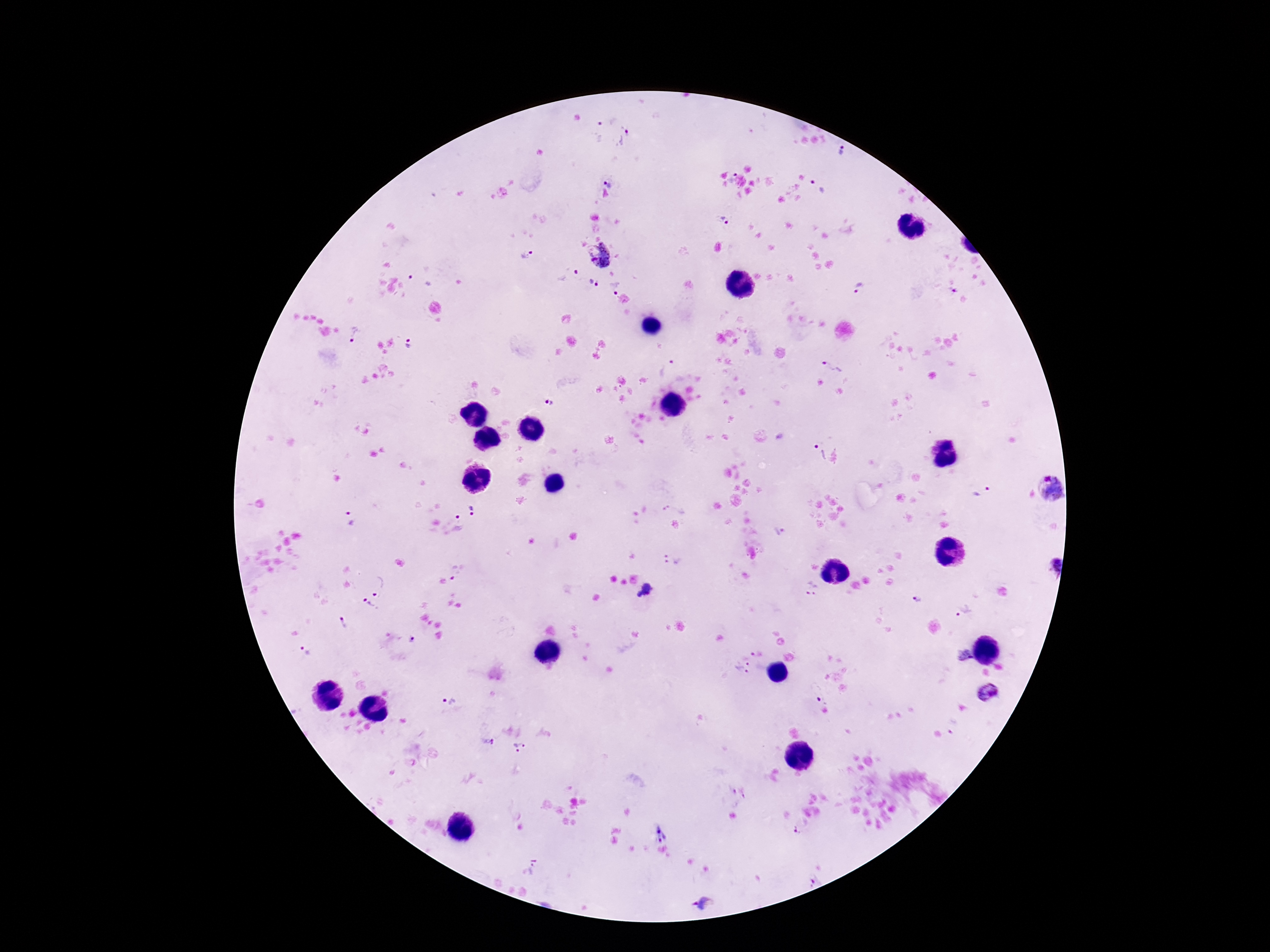
{
  "patient_malaria_status": "positive",
  "image_size": "1270×952 pixels",
  "stain": "Giemsa",
  "field_of_view": "single",
  "plasmodium_parasite_locations": "approximate object centers, in pixels from the top-left corner: (x=598, y=130), (x=627, y=138), (x=843, y=151), (x=731, y=176), (x=610, y=180), (x=819, y=185), (x=724, y=220), (x=597, y=253), (x=528, y=254), (x=567, y=275), (x=420, y=279), (x=592, y=283), (x=616, y=287), (x=858, y=288), (x=951, y=291), (x=354, y=336), (x=409, y=343), (x=666, y=366), (x=832, y=366), (x=551, y=403), (x=816, y=451), (x=1051, y=488), (x=982, y=490), (x=678, y=507), (x=474, y=510), (x=351, y=518), (x=459, y=520), (x=780, y=532), (x=672, y=560), (x=1054, y=565), (x=458, y=571), (x=382, y=584), (x=646, y=588), (x=812, y=588), (x=918, y=598), (x=367, y=606), (x=964, y=611), (x=345, y=621), (x=414, y=640), (x=305, y=652), (x=751, y=654), (x=965, y=656), (x=742, y=667), (x=988, y=692), (x=449, y=700), (x=488, y=743), (x=519, y=747), (x=661, y=830), (x=796, y=831), (x=528, y=870), (x=813, y=881), (x=705, y=903)",
  "capture": "smartphone camera through the microscope eyepiece",
  "magnification": "100x",
  "preparation": "thick blood smear"
}